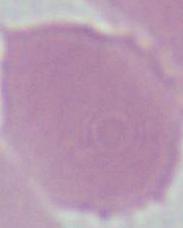
modality = micrograph
identification = erythrocyte
magnification = 1000x